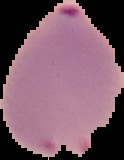
Summary:
  - Image size: 124×160 pixels
  - Result: malaria parasites detected
  - Preparation: thin blood smear
  - Image type: segmented cell region with the area outside set to black